Give the extent of all uninfected red blood cells.
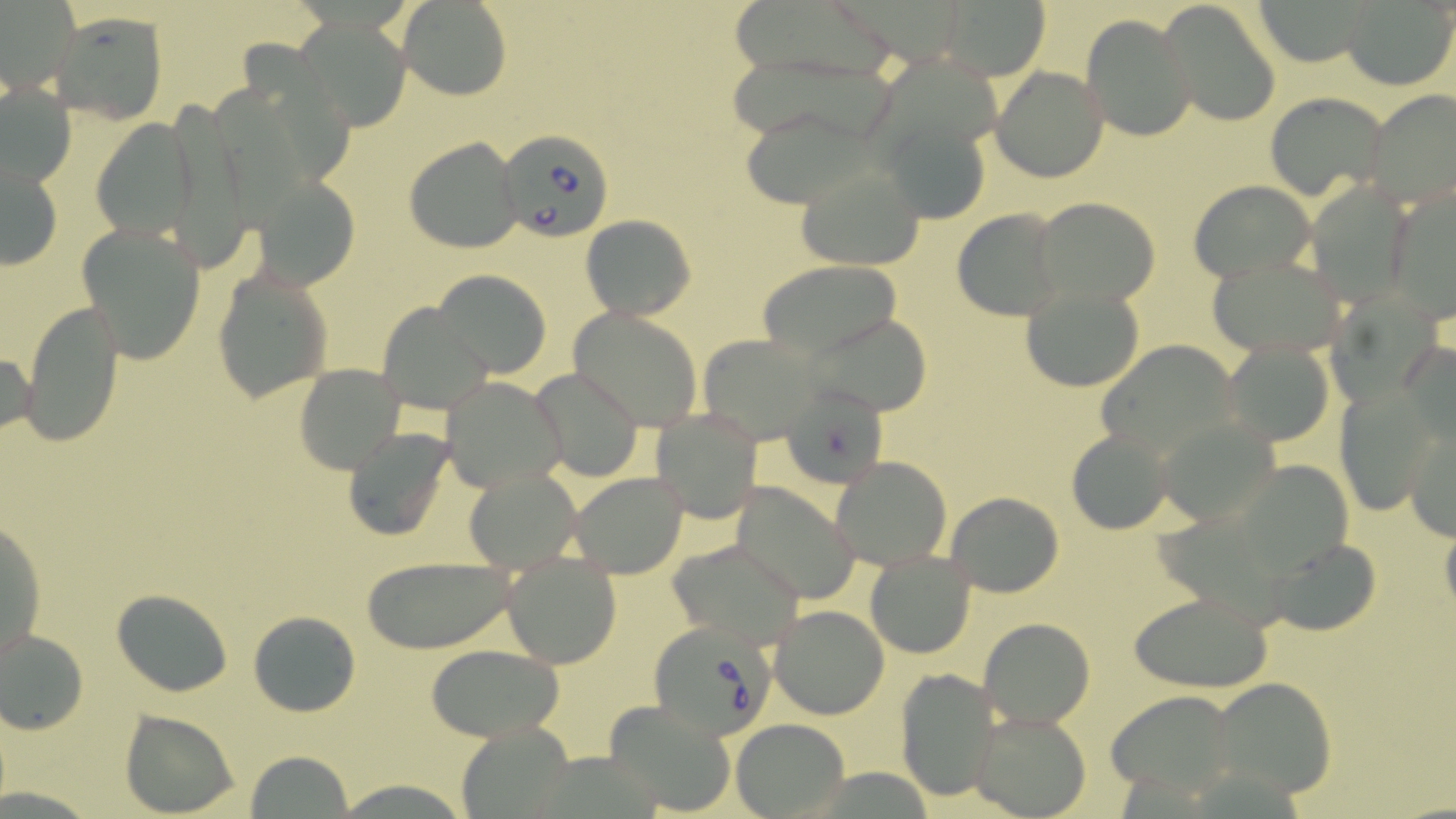

Approximate bounding boxes as (x1, y1, x2, y2) in pixels.
Uninfected red blood cells: (729, 0, 893, 81), (1251, 0, 1381, 66), (1158, 1, 1282, 127), (397, 2, 511, 101), (936, 2, 1053, 79), (1344, 2, 1454, 88), (46, 11, 169, 124), (1081, 13, 1195, 141), (297, 20, 409, 129), (241, 39, 351, 186), (872, 57, 1013, 155), (991, 66, 1109, 183), (1, 80, 76, 190), (220, 84, 300, 235), (1363, 90, 1456, 208), (1266, 91, 1389, 201), (159, 99, 254, 276), (739, 109, 883, 207), (880, 117, 990, 226), (93, 118, 197, 239), (404, 137, 523, 254), (2, 157, 64, 271), (794, 163, 926, 270), (255, 175, 363, 289), (1187, 180, 1317, 287), (1384, 187, 1456, 317), (1031, 197, 1161, 309), (952, 207, 1067, 322), (580, 214, 695, 319), (76, 221, 209, 364), (1207, 254, 1352, 359), (757, 260, 903, 359), (213, 265, 334, 402), (432, 270, 554, 376), (1020, 284, 1146, 391), (1318, 284, 1450, 411), (20, 301, 127, 443), (377, 301, 492, 413), (568, 307, 704, 431), (804, 313, 934, 416), (698, 334, 824, 440), (1221, 336, 1336, 447), (1095, 338, 1240, 459), (1399, 340, 1456, 452), (0, 346, 36, 446), (294, 364, 406, 475), (529, 365, 644, 482), (441, 375, 568, 492), (785, 385, 898, 488), (1333, 387, 1439, 517), (649, 408, 764, 522), (1158, 416, 1281, 526), (1402, 420, 1456, 541), (1065, 427, 1177, 534), (342, 429, 453, 541), (830, 456, 954, 569), (1231, 457, 1360, 583), (465, 466, 583, 573), (568, 471, 689, 579), (731, 482, 861, 603), (944, 491, 1065, 597), (2, 514, 47, 671), (1440, 522, 1456, 624), (1265, 537, 1383, 636), (665, 538, 806, 651), (863, 549, 977, 659), (501, 552, 622, 670), (358, 555, 523, 654), (111, 588, 235, 696), (1128, 588, 1275, 692), (768, 604, 891, 719), (248, 611, 361, 716), (978, 616, 1096, 729), (0, 626, 90, 735), (425, 645, 566, 742), (893, 668, 1001, 801), (1212, 675, 1339, 798), (1105, 688, 1240, 801), (605, 699, 739, 816), (118, 709, 241, 816), (968, 709, 1092, 818), (731, 719, 849, 815), (456, 724, 577, 815), (243, 750, 354, 818), (331, 777, 473, 817).

Babesia divergens-infected red blood cell locations: (497, 129, 614, 243), (651, 620, 776, 743). Slide-level diagnosis: Babesia divergens. May-Grünwald-Giemsa-stained preparation. Image is 1456×819 pixels. Light microscopy. Thin blood smear. Single field of view. 1000x magnification.